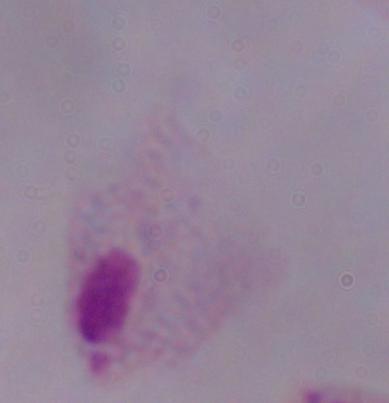

Summary:
  - Identification: trichomonad
  - Modality: photomicrograph
  - Magnification: 1000x